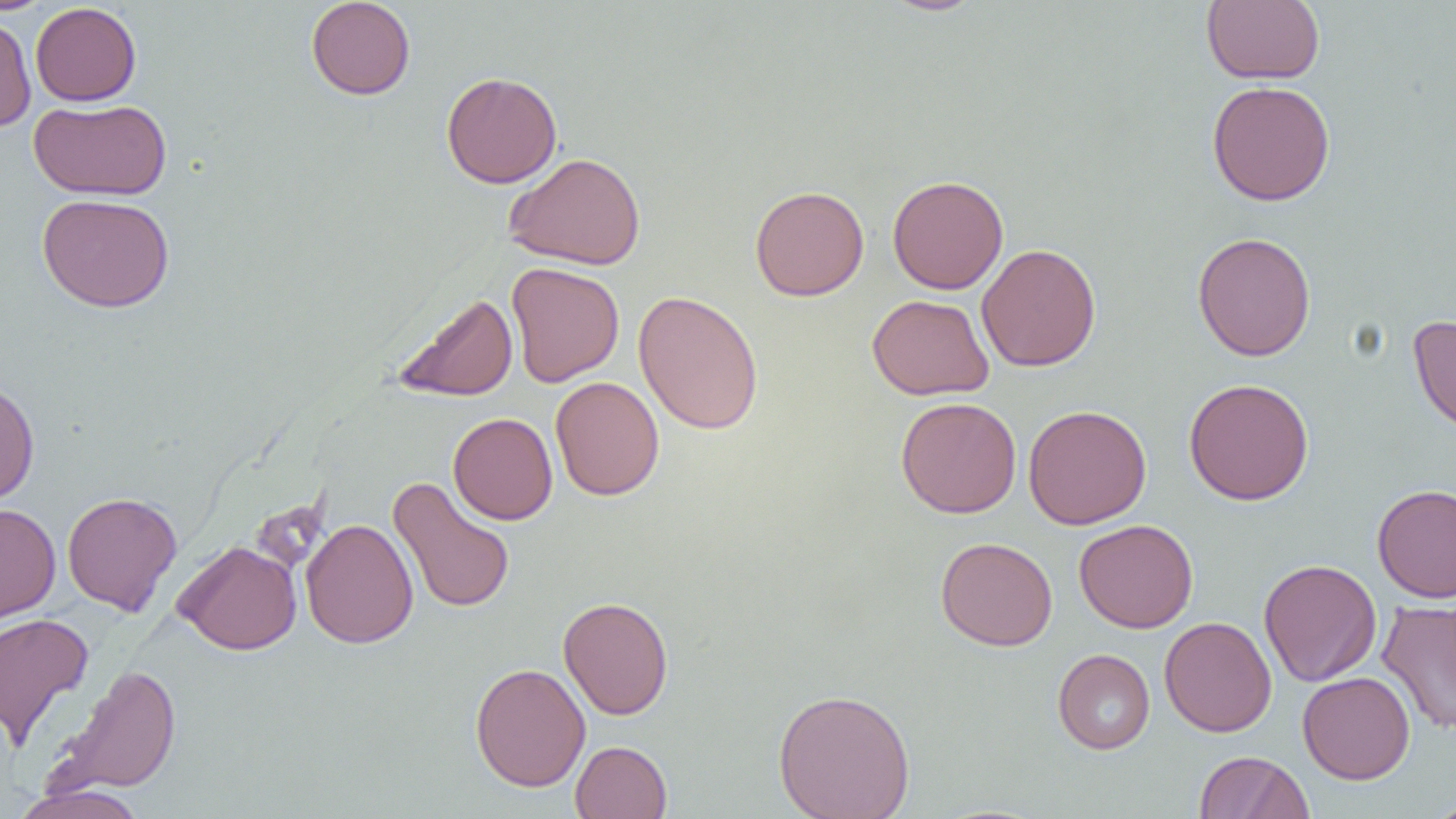

Summary:
  - Coordinate format: approximate bounding boxes as named x1/y1/x2/y2 corners in pixels
  - Uninfected red blood cell locations: (x1=305, y1=0, x2=416, y2=100), (x1=879, y1=0, x2=986, y2=16), (x1=1201, y1=0, x2=1325, y2=85), (x1=30, y1=2, x2=142, y2=106), (x1=0, y1=13, x2=37, y2=132), (x1=441, y1=71, x2=562, y2=188), (x1=1207, y1=80, x2=1335, y2=206), (x1=29, y1=98, x2=172, y2=200), (x1=503, y1=151, x2=646, y2=270), (x1=887, y1=175, x2=1009, y2=294), (x1=749, y1=185, x2=869, y2=301), (x1=37, y1=193, x2=175, y2=313), (x1=1192, y1=231, x2=1316, y2=361), (x1=976, y1=243, x2=1102, y2=372), (x1=506, y1=262, x2=625, y2=387), (x1=633, y1=290, x2=764, y2=435), (x1=392, y1=292, x2=518, y2=402), (x1=867, y1=294, x2=994, y2=400), (x1=1408, y1=314, x2=1456, y2=437), (x1=550, y1=376, x2=665, y2=501), (x1=0, y1=377, x2=40, y2=506), (x1=1184, y1=378, x2=1314, y2=505), (x1=895, y1=397, x2=1022, y2=518), (x1=1023, y1=404, x2=1152, y2=529), (x1=448, y1=412, x2=558, y2=525), (x1=387, y1=476, x2=516, y2=614), (x1=1371, y1=483, x2=1456, y2=603), (x1=62, y1=491, x2=182, y2=616), (x1=0, y1=503, x2=61, y2=624), (x1=301, y1=518, x2=418, y2=649), (x1=1074, y1=519, x2=1198, y2=633), (x1=935, y1=536, x2=1058, y2=651), (x1=172, y1=540, x2=302, y2=655), (x1=1258, y1=558, x2=1382, y2=687), (x1=558, y1=596, x2=674, y2=719), (x1=1377, y1=599, x2=1456, y2=734), (x1=0, y1=613, x2=94, y2=751), (x1=1159, y1=616, x2=1276, y2=737), (x1=1052, y1=648, x2=1155, y2=754), (x1=470, y1=662, x2=591, y2=792), (x1=50, y1=663, x2=182, y2=797), (x1=1297, y1=671, x2=1415, y2=785), (x1=773, y1=688, x2=916, y2=819), (x1=570, y1=740, x2=672, y2=818), (x1=1194, y1=751, x2=1312, y2=818), (x1=11, y1=784, x2=148, y2=819), (x1=1425, y1=798, x2=1456, y2=819)
  - Slide-level diagnosis: negative for blood parasites
  - Magnification: 1000x
  - Image size: 1456×819 pixels
  - Preparation: thin blood film
  - Field of view: single
  - Modality: light microscopy